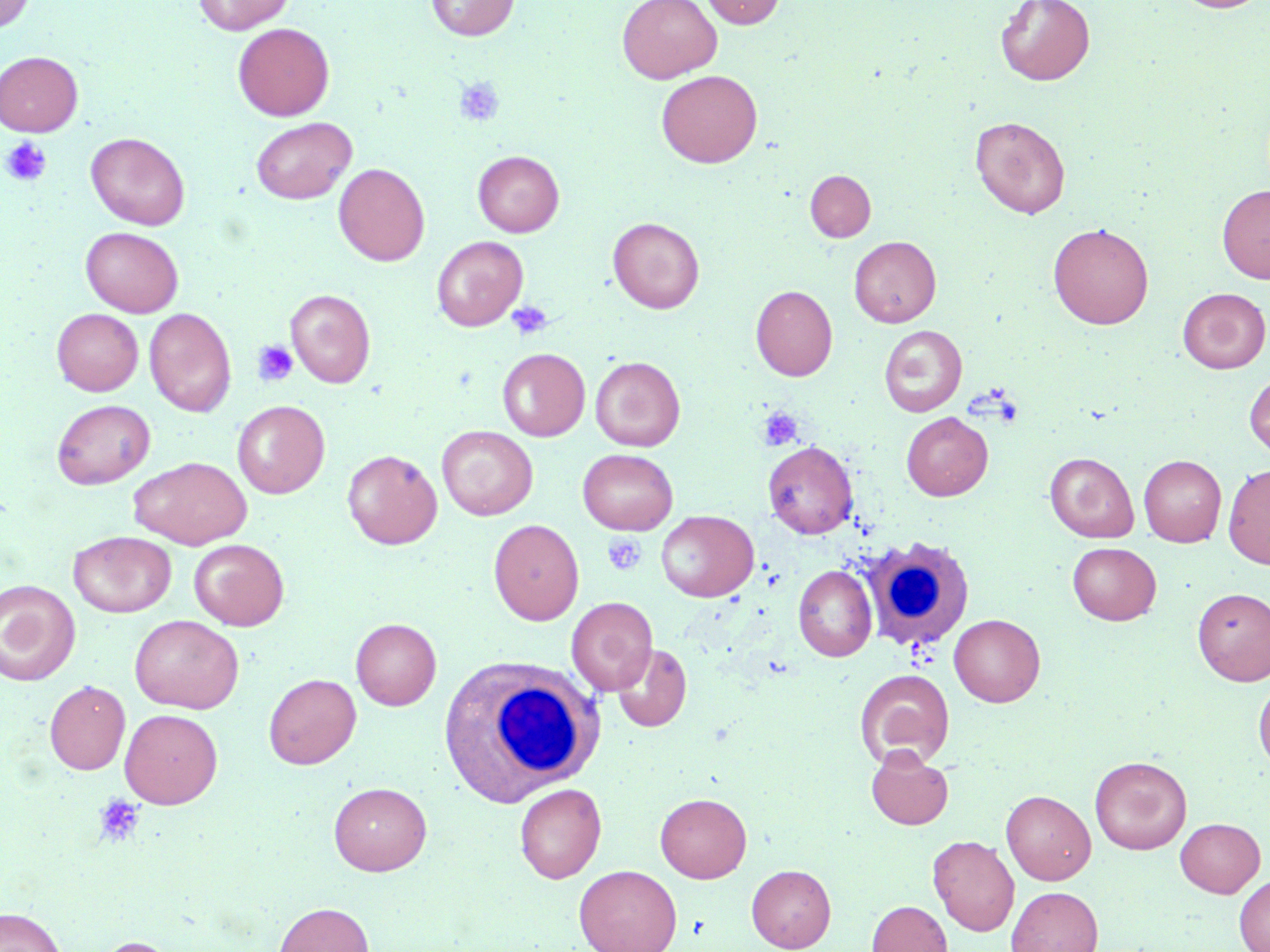
{
  "slide_level_diagnosis": "negative for blood parasites",
  "white_blood_cell_locations": "approximate bounding boxes as named x1/y1/x2/y2 corners in pixels: (x1=853, y1=537, x2=979, y2=659), (x1=437, y1=657, x2=600, y2=805)",
  "image_size": "1270×952 pixels",
  "platelet_locations": "approximate bounding boxes as named x1/y1/x2/y2 corners in pixels: (x1=454, y1=76, x2=505, y2=127), (x1=1, y1=137, x2=52, y2=186), (x1=506, y1=300, x2=552, y2=340), (x1=252, y1=339, x2=300, y2=386), (x1=757, y1=407, x2=803, y2=451), (x1=602, y1=534, x2=646, y2=576), (x1=94, y1=795, x2=145, y2=847)",
  "field_of_view": "one of a larger specimen",
  "magnification": "1000x",
  "modality": "optical microscopy",
  "uninfected_red_blood_cell_locations": "approximate bounding boxes as named x1/y1/x2/y2 corners in pixels: (x1=193, y1=0, x2=295, y2=35), (x1=426, y1=0, x2=519, y2=40), (x1=617, y1=0, x2=721, y2=83), (x1=701, y1=0, x2=785, y2=28), (x1=996, y1=0, x2=1095, y2=85), (x1=1173, y1=0, x2=1265, y2=13), (x1=0, y1=1, x2=35, y2=33), (x1=233, y1=23, x2=334, y2=120), (x1=0, y1=51, x2=83, y2=136), (x1=656, y1=70, x2=762, y2=167), (x1=971, y1=116, x2=1070, y2=218), (x1=250, y1=117, x2=357, y2=204), (x1=86, y1=133, x2=190, y2=230), (x1=473, y1=150, x2=564, y2=237), (x1=333, y1=163, x2=429, y2=266), (x1=805, y1=170, x2=876, y2=242), (x1=1217, y1=184, x2=1270, y2=284), (x1=608, y1=217, x2=704, y2=313), (x1=1048, y1=222, x2=1153, y2=329), (x1=81, y1=227, x2=183, y2=317), (x1=431, y1=236, x2=528, y2=331), (x1=849, y1=236, x2=940, y2=327), (x1=751, y1=285, x2=837, y2=381), (x1=1178, y1=288, x2=1269, y2=373), (x1=286, y1=289, x2=375, y2=387), (x1=52, y1=308, x2=143, y2=396), (x1=145, y1=308, x2=236, y2=416), (x1=879, y1=325, x2=967, y2=416), (x1=497, y1=348, x2=589, y2=441), (x1=591, y1=356, x2=685, y2=451), (x1=1245, y1=370, x2=1270, y2=460), (x1=52, y1=399, x2=156, y2=488), (x1=232, y1=400, x2=330, y2=498), (x1=902, y1=412, x2=993, y2=501), (x1=437, y1=426, x2=538, y2=520), (x1=763, y1=441, x2=858, y2=538), (x1=578, y1=449, x2=678, y2=534), (x1=342, y1=450, x2=442, y2=549), (x1=1045, y1=452, x2=1139, y2=542), (x1=1139, y1=455, x2=1226, y2=546), (x1=130, y1=456, x2=252, y2=549), (x1=1223, y1=465, x2=1270, y2=569), (x1=656, y1=510, x2=758, y2=601), (x1=489, y1=519, x2=584, y2=625), (x1=69, y1=531, x2=176, y2=617), (x1=189, y1=539, x2=289, y2=630), (x1=1067, y1=542, x2=1161, y2=625), (x1=793, y1=565, x2=877, y2=661), (x1=0, y1=581, x2=81, y2=685), (x1=1192, y1=587, x2=1270, y2=685), (x1=567, y1=597, x2=657, y2=695), (x1=949, y1=614, x2=1045, y2=706), (x1=129, y1=615, x2=244, y2=714), (x1=351, y1=618, x2=441, y2=709), (x1=612, y1=643, x2=692, y2=732), (x1=855, y1=668, x2=954, y2=769), (x1=264, y1=673, x2=361, y2=769), (x1=1253, y1=678, x2=1270, y2=774), (x1=45, y1=680, x2=130, y2=774), (x1=120, y1=708, x2=223, y2=808), (x1=866, y1=746, x2=954, y2=829), (x1=1090, y1=755, x2=1191, y2=854), (x1=328, y1=782, x2=432, y2=875), (x1=514, y1=783, x2=606, y2=883), (x1=1001, y1=790, x2=1096, y2=884), (x1=655, y1=792, x2=751, y2=882), (x1=1175, y1=817, x2=1265, y2=897), (x1=928, y1=835, x2=1019, y2=935), (x1=574, y1=864, x2=682, y2=952), (x1=746, y1=864, x2=836, y2=951), (x1=1234, y1=874, x2=1270, y2=952), (x1=1007, y1=886, x2=1103, y2=952), (x1=866, y1=900, x2=952, y2=952), (x1=274, y1=902, x2=374, y2=952), (x1=0, y1=907, x2=65, y2=952), (x1=94, y1=936, x2=180, y2=952)",
  "stain": "May-Grünwald-Giemsa",
  "preparation": "thin blood smear"
}